Classify this cell by malaria status.
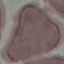

It is uninfected.

preparation = thin smear
stain = Giemsa
capture = smartphone through the microscope eyepiece
image type = automatically extracted cell patch, resized to 64 × 64 pixels